Classify this cell by malaria status.
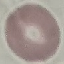
Uninfected.

Summary:
  - Stain: Giemsa
  - Preparation: thin blood smear
  - Image type: cell patch, automatically extracted from a larger field of view and resized to 64 × 64 pixels
  - Capture: smartphone through the microscope eyepiece